Locate every blood parasite and identify its species.
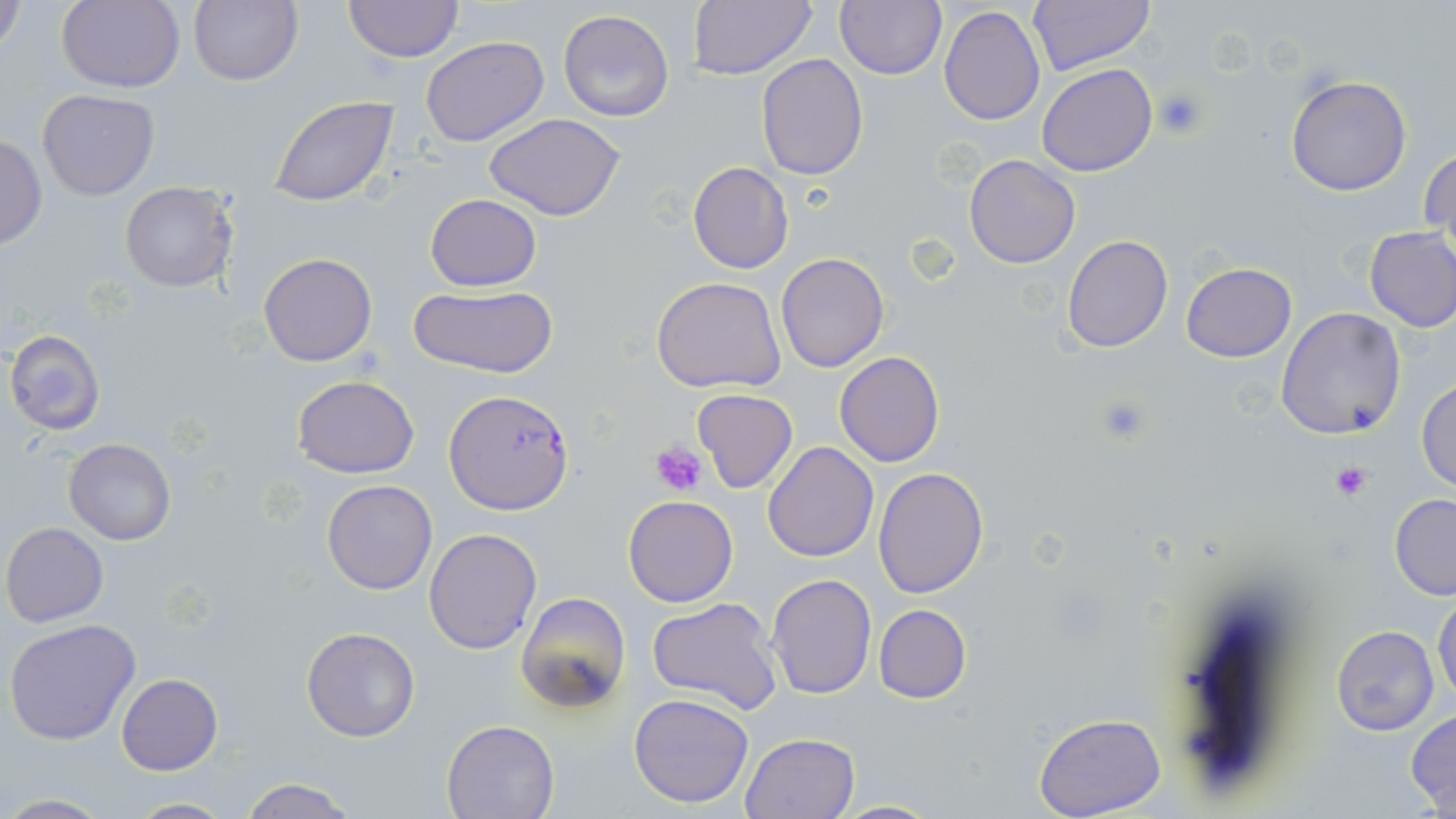
Approximate bounding boxes as [x1, y1, x2, y2] in pixels.
Plasmodium falciparum-infected red blood cells: [437, 389, 567, 514].
No Plasmodium ovale, Plasmodium malariae, Plasmodium vivax, Babesia divergens, or Trypanosoma brucei observed.

Summary:
  - Platelet locations: [1154, 88, 1208, 139], [1093, 393, 1155, 447], [648, 442, 708, 496], [1331, 460, 1372, 501]
  - Uninfected red blood cell locations: [1, 0, 27, 63], [57, 0, 185, 94], [189, 0, 305, 87], [344, 0, 463, 62], [690, 0, 817, 80], [1028, 0, 1156, 76], [834, 1, 947, 79], [938, 7, 1045, 127], [557, 9, 675, 123], [420, 36, 548, 148], [755, 53, 868, 179], [1038, 64, 1156, 177], [1285, 75, 1411, 196], [37, 89, 159, 200], [269, 95, 399, 204], [483, 114, 628, 220], [1, 133, 48, 250], [1421, 144, 1455, 258], [964, 154, 1080, 268], [689, 162, 793, 274], [119, 182, 238, 294], [425, 194, 541, 290], [1363, 226, 1456, 333], [1062, 234, 1173, 353], [258, 252, 378, 367], [775, 252, 889, 372], [1181, 263, 1296, 363], [651, 276, 786, 392], [407, 284, 558, 380], [1276, 307, 1406, 441], [5, 330, 107, 436], [834, 351, 944, 466], [292, 375, 420, 477], [1416, 376, 1456, 494], [692, 389, 799, 492], [63, 437, 176, 546], [763, 441, 878, 562], [873, 467, 991, 598], [322, 479, 438, 595], [1389, 494, 1456, 599], [623, 495, 738, 607], [2, 522, 108, 627], [424, 527, 543, 654], [765, 573, 877, 699], [514, 591, 630, 717], [1433, 593, 1455, 706], [646, 598, 785, 716], [874, 604, 971, 703], [5, 619, 140, 745], [1332, 625, 1439, 735], [300, 627, 421, 742], [116, 673, 222, 775], [628, 693, 756, 808], [1407, 709, 1456, 813], [1034, 712, 1166, 818], [442, 718, 561, 818], [740, 733, 859, 819], [239, 777, 359, 819], [0, 794, 115, 817], [124, 796, 233, 817], [827, 799, 944, 818]
  - Slide-level diagnosis: Plasmodium falciparum
  - Image size: 1456×819 pixels
  - Preparation: thin blood smear
  - Modality: optical microscopy
  - Field of view: single
  - Stain: May-Grünwald-Giemsa
  - Magnification: 1000x